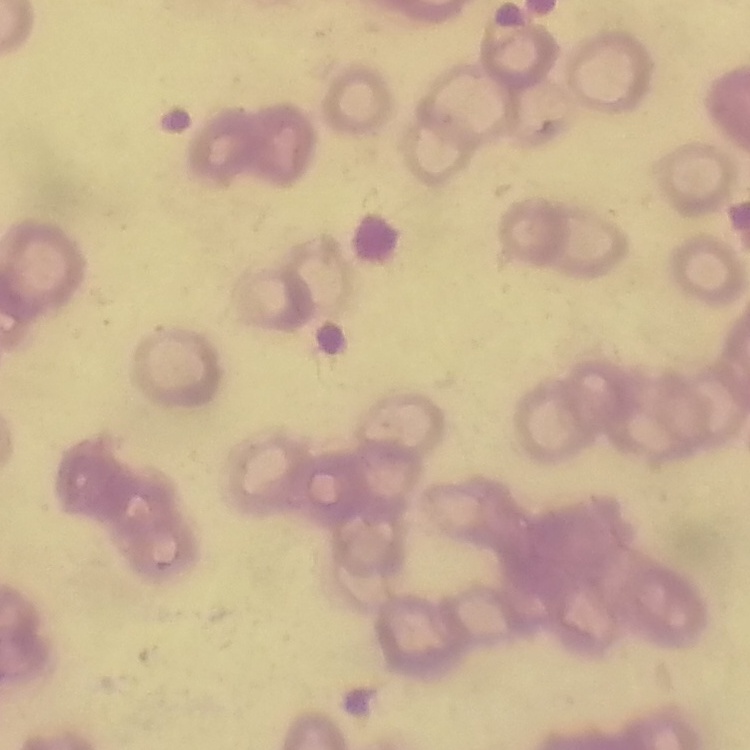
The red blood cells exhibit rouleaux formation. Field's or Giemsa stain. Thin peripheral smear. One tile cut from a larger photomicrograph.